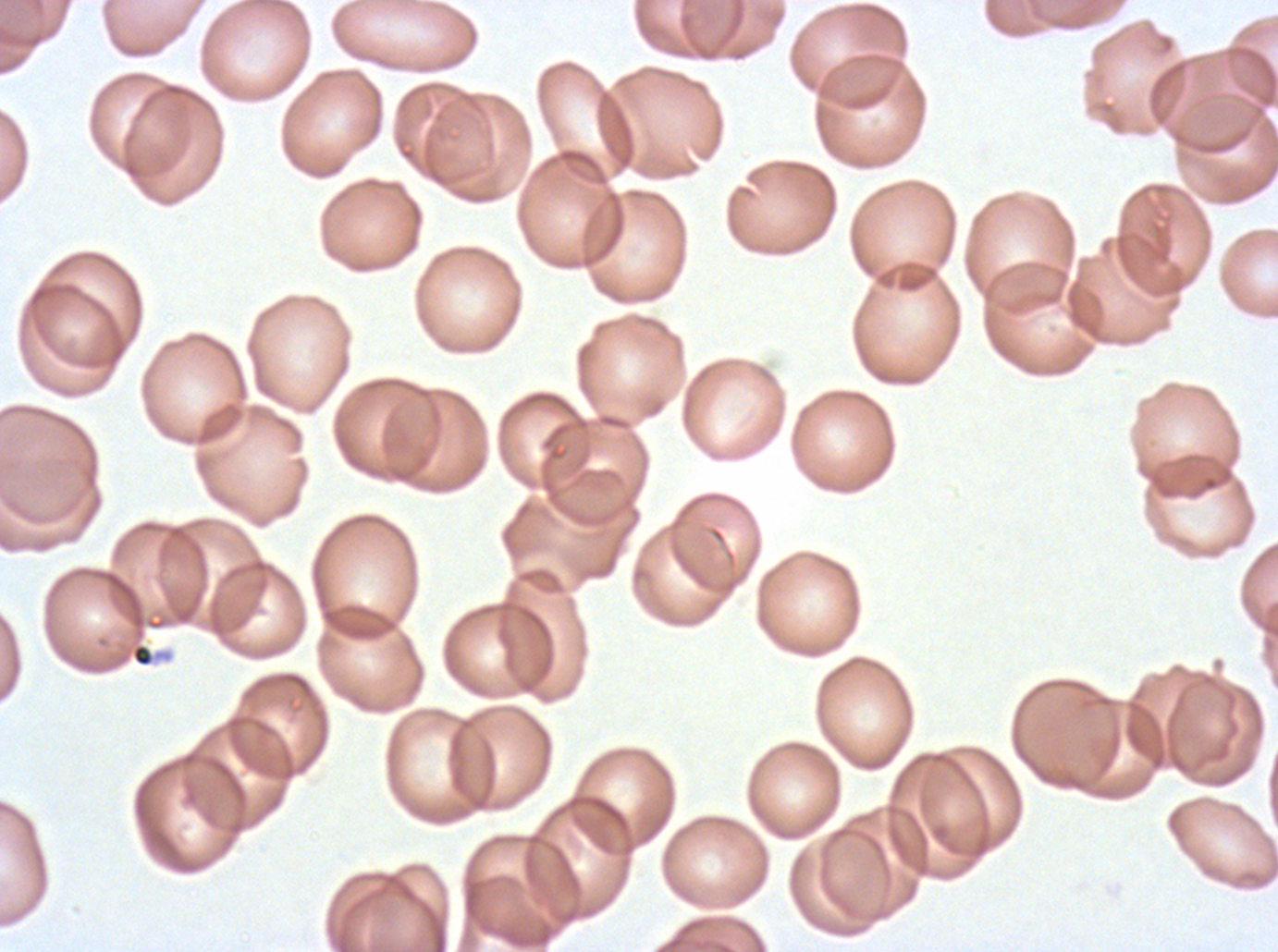
notation = approximate bounding rectangles given as corner coordinates in pixels from the top-left
debris locations = (x1=92, y1=568, x2=167, y2=640)
field of view = one sub-image of a larger composite
specimen = Plasmodium falciparum cultured ex vivo for 24 to 48 hours, from a patient in The Gambia
stain = Giemsa
image size = 1278×952 pixels
preparation = thin blood smear